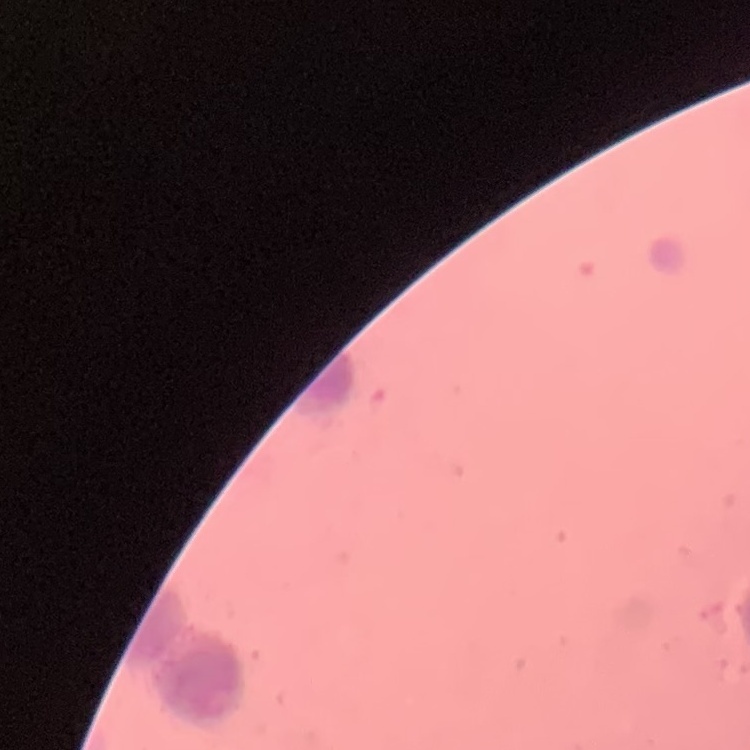
erythrocyte morphology = rouleaux formation
preparation = thin peripheral smear
image type = square crop of a larger photomicrograph
stain = Field's or Giemsa